Locate every Plasmodium vivax-infected red blood cell.
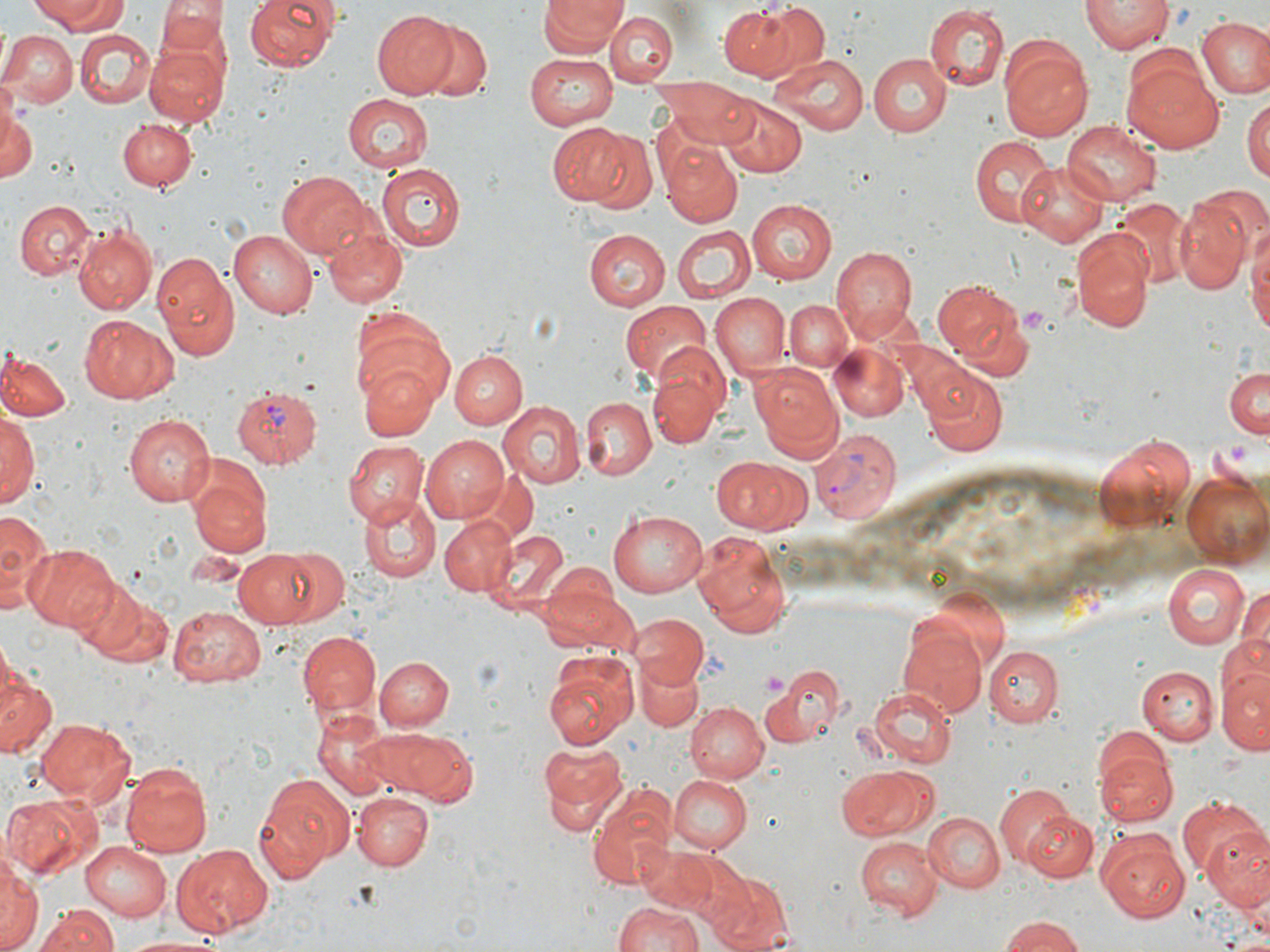

Approximate bounding boxes as (x1,y1)-(x2,y2) corner pairs in pixels.
Plasmodium vivax-infected red blood cells: (230,386)-(322,464), (811,427)-(902,525).

Uninfected red blood cell locations: (31,0)-(127,33), (245,0)-(341,71), (538,0)-(625,56), (1081,0)-(1171,54), (152,2)-(230,69), (718,5)-(798,80), (759,5)-(830,76), (923,5)-(1009,90), (374,9)-(459,99), (606,12)-(677,84), (1196,16)-(1270,100), (413,20)-(492,100), (1,28)-(77,109), (76,30)-(156,108), (997,34)-(1094,141), (144,43)-(228,125), (1122,51)-(1223,154), (527,52)-(622,129), (769,52)-(870,137), (868,54)-(951,136), (1,73)-(19,156), (662,79)-(759,148), (341,93)-(435,172), (1243,95)-(1270,186), (717,96)-(805,176), (0,98)-(38,183), (117,117)-(197,191), (1061,120)-(1162,206), (546,122)-(643,208), (968,133)-(1055,229), (660,139)-(743,228), (1015,162)-(1109,247), (375,165)-(463,249), (279,171)-(369,258), (1174,192)-(1253,298), (747,199)-(837,285), (1110,199)-(1193,288), (14,200)-(96,280), (319,218)-(409,311), (1246,218)-(1270,341), (73,224)-(156,315), (672,224)-(753,303), (1067,228)-(1154,332), (229,229)-(318,318), (582,229)-(669,309), (831,244)-(918,341), (149,249)-(242,361), (932,277)-(1031,376), (709,294)-(790,379), (621,300)-(711,383), (785,300)-(854,371), (78,315)-(178,404), (350,315)-(456,411), (830,345)-(908,422), (0,348)-(70,422), (450,349)-(525,429), (647,354)-(728,447), (446,355)-(566,459), (361,361)-(438,443), (751,363)-(844,456), (1224,366)-(1270,439), (922,371)-(1007,457), (580,397)-(655,480), (499,402)-(586,489), (1,408)-(39,509), (121,412)-(215,508), (1094,432)-(1199,538), (420,434)-(510,521), (343,440)-(428,528), (710,455)-(806,533), (185,460)-(273,559), (1182,471)-(1269,567), (360,495)-(440,581), (607,508)-(708,597), (0,510)-(54,616), (439,516)-(515,595), (480,525)-(573,615), (692,530)-(794,639), (27,544)-(120,631), (272,547)-(349,623), (233,549)-(327,628), (1163,562)-(1251,648), (539,574)-(638,657), (68,578)-(166,667), (1238,583)-(1270,669), (168,604)-(266,685), (630,613)-(709,686), (899,626)-(988,719), (297,630)-(380,717), (986,645)-(1064,728), (543,650)-(639,750), (377,656)-(454,731), (635,662)-(703,732), (0,664)-(57,759), (1219,665)-(1270,754), (1138,666)-(1216,745), (765,668)-(845,747), (865,686)-(957,768), (685,700)-(769,782), (310,710)-(397,800), (34,716)-(135,806), (364,728)-(479,805), (534,738)-(629,837), (1096,748)-(1176,828), (120,759)-(213,856), (836,765)-(934,841), (251,772)-(353,882), (669,774)-(748,853), (667,777)-(761,918), (585,782)-(678,891), (994,783)-(1076,868), (351,791)-(435,871), (3,794)-(100,881), (1175,797)-(1267,879), (920,811)-(1003,892), (1024,811)-(1098,882), (1201,822)-(1270,907), (1096,830)-(1190,922), (854,837)-(941,918), (80,839)-(175,920), (169,845)-(273,937), (1,846)-(39,952), (642,846)-(726,918), (682,856)-(759,935), (710,873)-(795,952), (610,900)-(704,952), (38,906)-(118,952), (998,915)-(1087,952), (117,933)-(226,951). Platelet locations: (760,670)-(790,700). Slide-level diagnosis: Plasmodium vivax. Thin blood smear. Light microscopy. 1000x magnification. Single field of view. Image is 1270×952 pixels. May-Grünwald-Giemsa-stained preparation.